Classify this cell by malaria status.
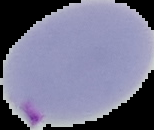

It is parasitized.

{
  "image_type": "cell region segmented out of the field of view; surrounding area masked to black",
  "preparation": "thin blood film",
  "image_size": "154×130 pixels"
}